Draw a bounding box around every leukocyte (white blood cell).
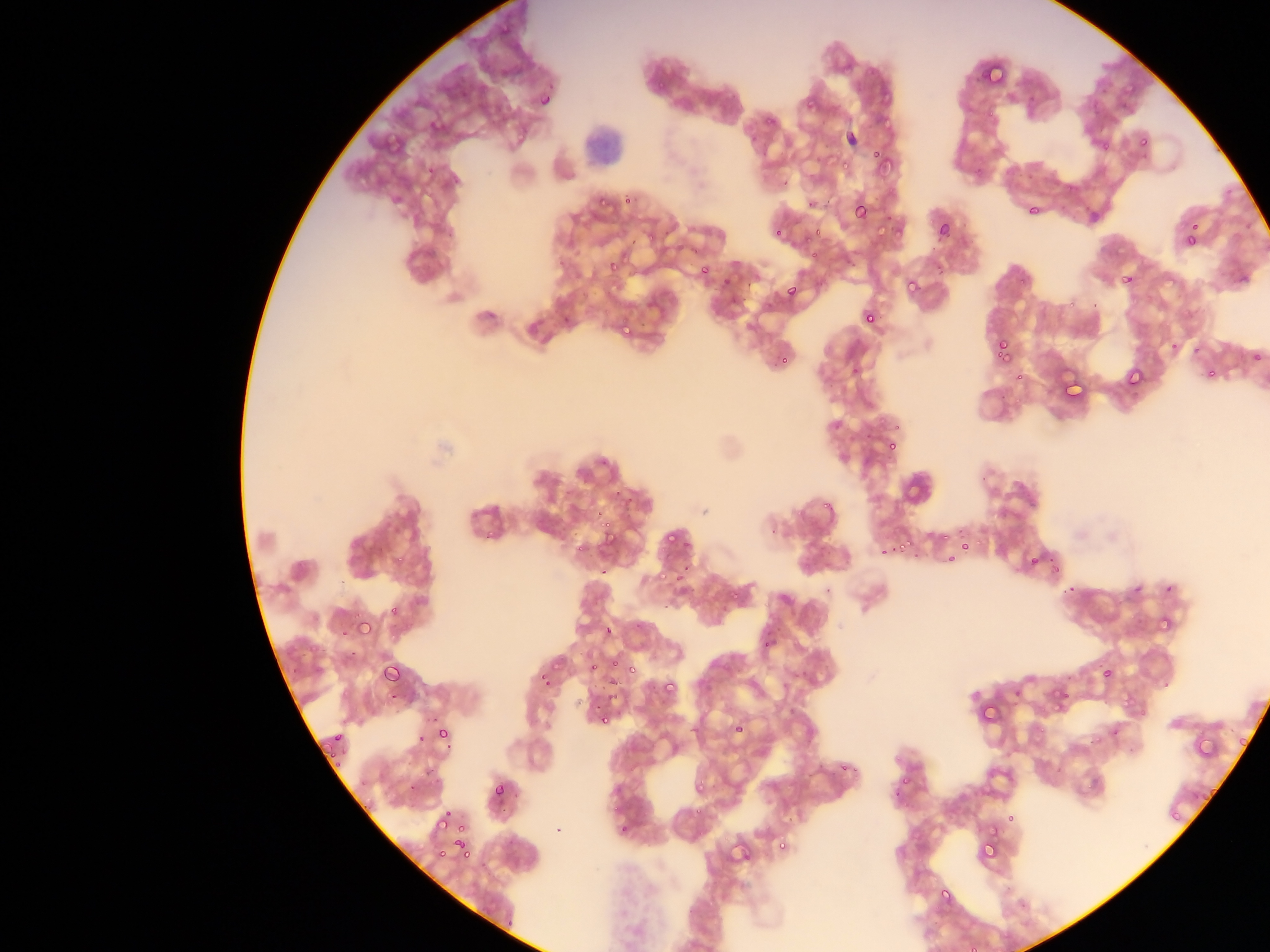
No leukocytes observed.

Approximate bounding boxes as (left, top, right, bottom) in pixels. Plasmodium parasite locations: (989, 62, 1011, 79), (1124, 81, 1135, 92), (658, 82, 666, 92), (535, 90, 559, 116), (805, 96, 821, 108), (765, 108, 781, 124), (985, 108, 995, 116), (514, 131, 525, 141), (1141, 136, 1151, 146), (1102, 140, 1110, 151), (871, 150, 883, 159), (874, 159, 897, 178), (840, 161, 850, 169), (974, 165, 984, 174), (425, 167, 434, 174), (595, 194, 609, 204), (622, 196, 633, 206), (848, 200, 872, 226), (1026, 201, 1038, 217), (932, 218, 954, 244), (875, 220, 889, 235), (893, 220, 903, 243), (1189, 220, 1199, 235), (816, 225, 827, 235), (771, 228, 782, 236), (644, 230, 656, 242), (805, 234, 814, 243), (1185, 238, 1196, 246), (691, 245, 701, 255), (809, 252, 818, 261), (621, 253, 631, 262), (606, 256, 620, 271), (696, 264, 716, 287), (720, 273, 735, 291), (902, 275, 925, 301), (1120, 275, 1132, 286), (1016, 276, 1029, 289), (781, 281, 803, 306), (1065, 298, 1078, 308), (859, 306, 880, 330), (602, 307, 612, 317), (621, 327, 631, 338), (1170, 335, 1178, 354), (993, 338, 1013, 362), (1193, 347, 1201, 356), (1250, 347, 1268, 368), (780, 355, 790, 364), (1123, 364, 1148, 392), (1207, 366, 1218, 379), (850, 369, 860, 375), (1013, 371, 1025, 379), (1065, 377, 1086, 400), (894, 425, 900, 433), (887, 442, 896, 450), (821, 503, 831, 509), (597, 518, 621, 550), (484, 530, 494, 541), (944, 530, 954, 540), (667, 532, 677, 544), (900, 536, 913, 548), (960, 539, 970, 549), (880, 544, 885, 554), (575, 547, 584, 552), (1026, 552, 1045, 573), (397, 554, 407, 563), (946, 555, 955, 563), (1050, 563, 1060, 576), (676, 571, 685, 581), (657, 574, 667, 581), (1066, 580, 1078, 592), (730, 591, 743, 602), (389, 606, 400, 615), (356, 615, 372, 634), (1159, 618, 1173, 632), (601, 623, 615, 638), (341, 629, 347, 639), (763, 641, 774, 650), (308, 646, 316, 654), (379, 658, 405, 687), (590, 658, 602, 675), (611, 660, 621, 669), (1099, 665, 1117, 685), (627, 667, 639, 678), (537, 672, 548, 681), (658, 678, 680, 702), (544, 680, 556, 686), (1057, 692, 1070, 704), (1120, 697, 1131, 704), (983, 703, 1000, 718), (1057, 703, 1065, 714), (1135, 710, 1149, 718), (600, 711, 615, 724), (429, 714, 438, 723), (730, 720, 750, 740), (1037, 721, 1047, 734), (437, 726, 451, 737), (1114, 728, 1126, 736), (1194, 729, 1219, 755), (333, 730, 343, 740), (414, 732, 423, 745), (1088, 732, 1104, 742), (1238, 734, 1251, 747), (317, 740, 331, 758), (328, 755, 338, 760), (891, 755, 901, 764), (333, 761, 343, 771), (851, 766, 860, 773), (899, 774, 910, 787), (491, 780, 511, 802), (1084, 781, 1094, 790), (697, 783, 706, 789), (1207, 785, 1216, 794), (1197, 791, 1207, 800), (892, 792, 900, 798), (1169, 806, 1182, 823), (443, 809, 452, 817), (693, 809, 702, 815), (1006, 812, 1019, 824), (434, 817, 448, 829), (455, 819, 466, 831), (762, 822, 771, 832), (619, 824, 630, 831), (977, 833, 1004, 864), (454, 839, 465, 848), (777, 839, 792, 850), (435, 846, 451, 860), (461, 847, 472, 859), (938, 888, 952, 903), (965, 944, 977, 952) | approximate (x, y) pixel centers of objects too small to bound: (841, 770). Thin blood film. Image is 1270×952 pixels. Single field of view. Mobile-phone photograph taken through the microscope. Sample from Ghana.